Name the parasite shown.
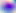

This is Toxoplasma gondii.

Summary:
  - Magnification: 400x
  - Modality: photomicrograph